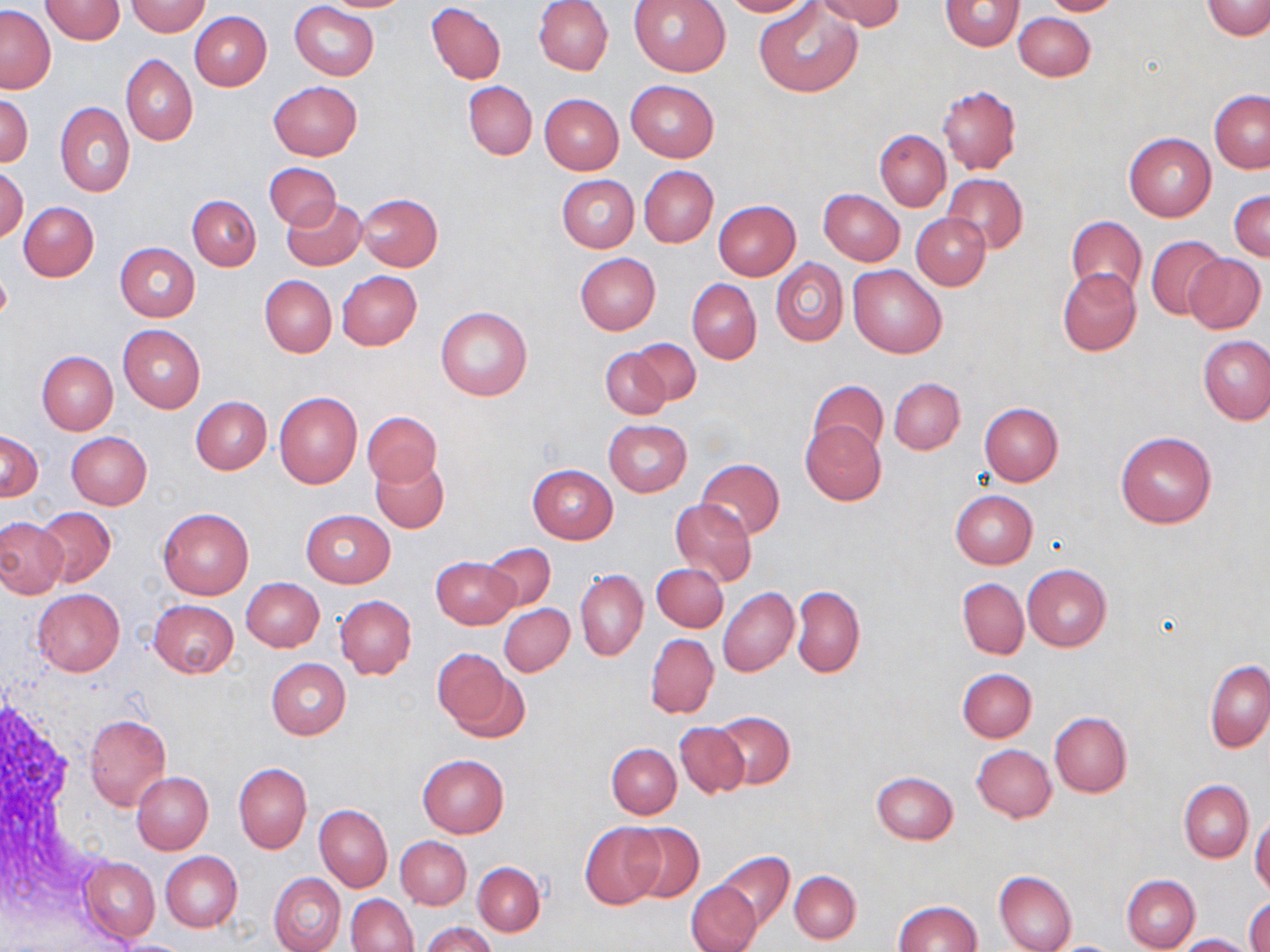
Approximate bounding boxes as (x1,y1)-(x2,y2) corner pairs in pixels. Uninfected red blood cell locations: (42,0)-(125,44), (316,0)-(414,12), (534,0)-(613,75), (628,0)-(731,76), (721,0)-(814,17), (815,0)-(905,31), (939,0)-(1023,51), (1039,0)-(1124,17), (1202,0)-(1270,39), (127,1)-(211,36), (290,2)-(379,81), (426,3)-(506,83), (755,3)-(862,97), (1,6)-(56,94), (190,11)-(271,90), (1014,11)-(1095,81), (121,54)-(197,146), (625,80)-(719,161), (267,81)-(362,161), (463,81)-(537,161), (938,86)-(1021,175), (1209,90)-(1270,173), (539,93)-(624,174), (549,93)-(629,252), (0,94)-(33,166), (54,102)-(135,197), (875,130)-(950,211), (1124,133)-(1216,222), (265,162)-(340,230), (1,166)-(27,242), (639,166)-(718,248), (942,173)-(1029,254), (558,175)-(638,252), (819,188)-(904,266), (1230,190)-(1270,261), (357,193)-(443,271), (188,196)-(261,270), (280,197)-(367,271), (714,200)-(800,280), (19,202)-(98,281), (911,212)-(990,290), (1067,215)-(1147,300), (1147,235)-(1227,320), (115,242)-(201,321), (575,253)-(660,335), (1184,253)-(1265,334), (771,258)-(847,346), (847,264)-(947,358), (1058,269)-(1141,356), (336,271)-(422,350), (259,275)-(336,357), (687,279)-(761,363), (436,306)-(532,401), (118,325)-(205,413), (1198,335)-(1270,424), (628,337)-(703,406), (601,345)-(673,419), (36,351)-(117,435), (888,377)-(964,454), (808,378)-(888,460), (274,393)-(363,488), (191,396)-(272,475), (979,402)-(1062,486), (363,410)-(441,487), (603,420)-(692,497), (800,421)-(887,504), (0,430)-(42,502), (65,432)-(151,510), (1117,432)-(1216,528), (371,457)-(449,533), (695,458)-(785,540), (527,465)-(618,543), (950,490)-(1037,568), (670,498)-(756,589), (35,506)-(116,587), (159,507)-(254,598), (300,509)-(396,587), (0,518)-(67,598), (483,544)-(556,610), (431,557)-(519,630), (651,564)-(728,632), (1022,564)-(1111,652), (576,570)-(647,661), (957,577)-(1029,660), (242,578)-(324,651), (792,586)-(864,677), (31,588)-(125,675), (718,588)-(798,676), (336,596)-(416,678), (148,599)-(238,678), (499,603)-(574,677), (645,633)-(719,719), (432,648)-(515,733), (266,658)-(350,741), (1205,660)-(1270,752), (957,668)-(1037,742), (711,711)-(794,789), (1049,712)-(1131,797), (85,714)-(171,809), (674,721)-(750,798), (607,743)-(681,819), (971,745)-(1056,822), (417,754)-(509,836), (234,763)-(312,853), (131,771)-(213,855), (871,772)-(958,844), (1179,780)-(1253,862), (315,804)-(392,891), (1250,814)-(1270,896), (579,821)-(665,909), (624,822)-(705,903), (395,837)-(472,910), (717,851)-(795,932), (161,852)-(242,932), (80,856)-(160,943), (473,862)-(544,936), (994,870)-(1078,952), (789,871)-(860,944), (269,872)-(346,952), (1123,874)-(1200,951), (686,881)-(762,952), (347,894)-(419,952), (1246,898)-(1270,952), (892,901)-(982,952), (422,921)-(496,952), (1173,933)-(1256,952), (109,939)-(196,951). Slide-level diagnosis: negative for blood parasites. Image is 1270×952 pixels. May-Grünwald-Giemsa-stained preparation. Thin blood smear. Light microscopy. Captured at 1000x magnification. Single field of view.